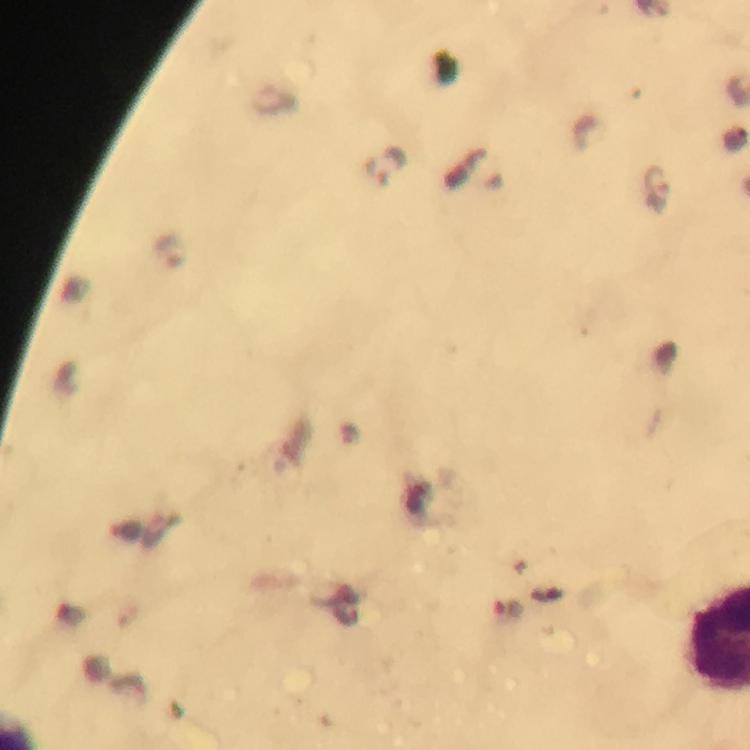 Approximate centers as {x, y} in pixels. Plasmodium parasite locations: {384, 166}, {656, 189}, {169, 252}. 100x magnification. From a malaria diagnostic workup. Smartphone photograph taken through a microscope. Cropped region of a single field of view. Immersion oil was used. Image is 750×750 pixels. Thick smear. Giemsa-stained preparation.